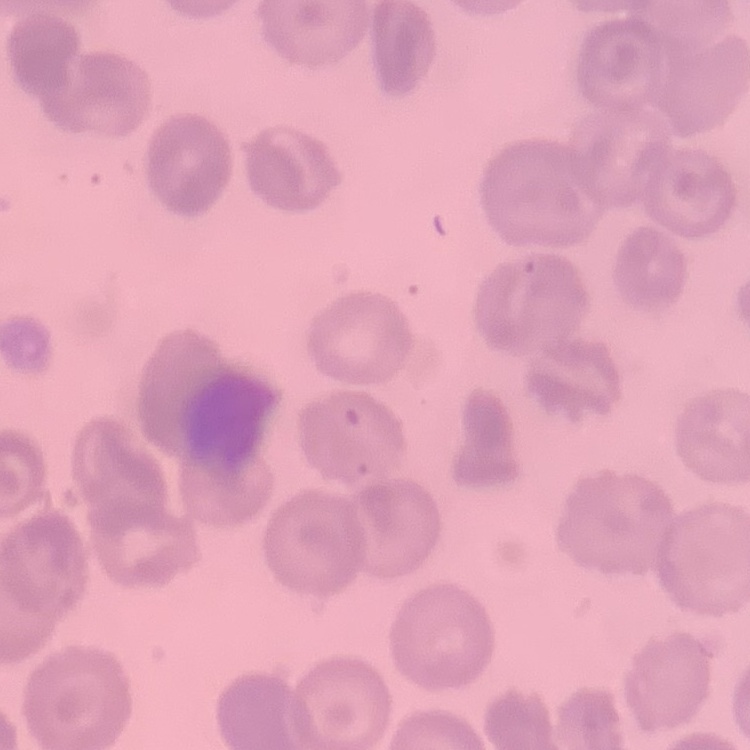

The erythrocytes exhibit no rouleaux formation. One tile cut from a larger photomicrograph. Thin peripheral smear. Field's or Giemsa stain.